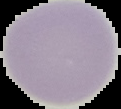
Summary:
  - Image type: cell region segmented out of the field of view; surrounding area masked to black
  - Image size: 121×109 pixels
  - Preparation: thin blood smear
  - Result: no malaria parasites seen